Assess this cell for malaria.
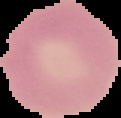
It is uninfected.

Summary:
  - Image size: 121×118 pixels
  - Preparation: thin blood smear
  - Image type: segmented cell region on a black background